Assess this cell for malaria.
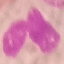

Uninfected.

Summary:
  - Preparation: thin blood film
  - Stain: Giemsa
  - Capture: smartphone camera at the microscope eyepiece
  - Image type: cell patch, automatically extracted from a larger field of view and resized to 64 × 64 pixels